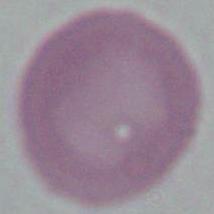

A red blood cell is seen. Captured at 1000x magnification. Photomicrograph.